Describe the morphology of the red blood cells.
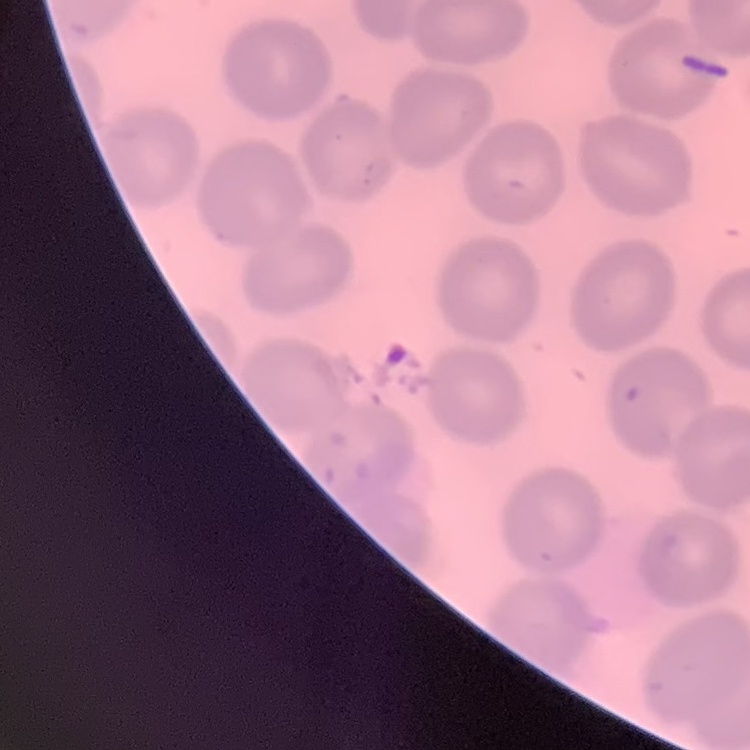
No rouleaux formation.

Stained with either Field's or Giemsa. Square crop of a larger photomicrograph. Thin peripheral smear.